Name the parasite shown.
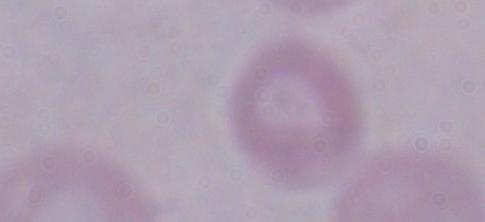

A trypanosome.

Summary:
  - Modality: micrograph
  - Magnification: 1000x